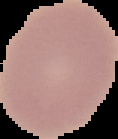

Cell region segmented out of the field of view; the surrounding area is masked to black. Malaria status: uninfected. From a thin blood smear. Image is 118×139 pixels.